Assess the morphology of the red blood cells.
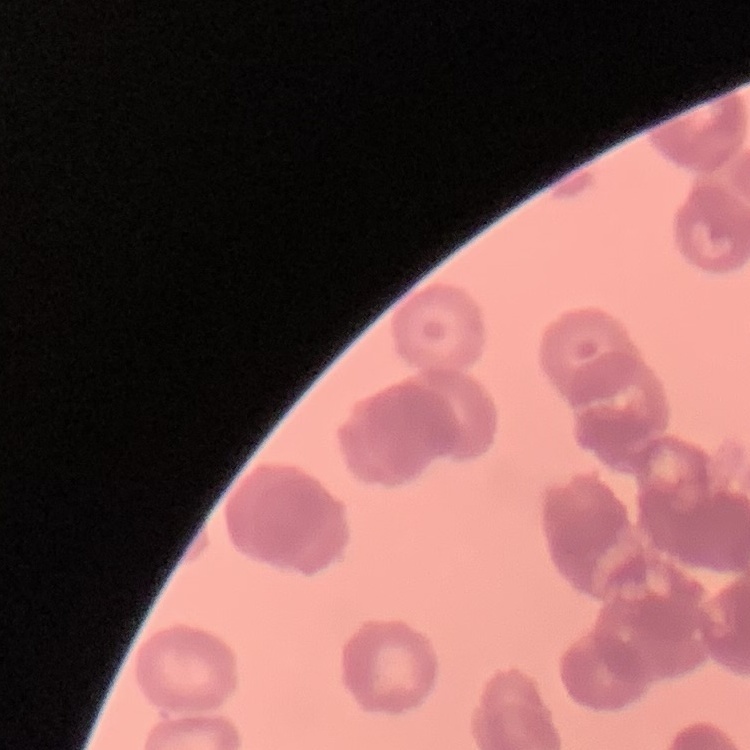
They show rouleaux formation.

Summary:
  - Stain: Field's or Giemsa
  - Image type: square crop of a larger photomicrograph
  - Preparation: thin peripheral smear